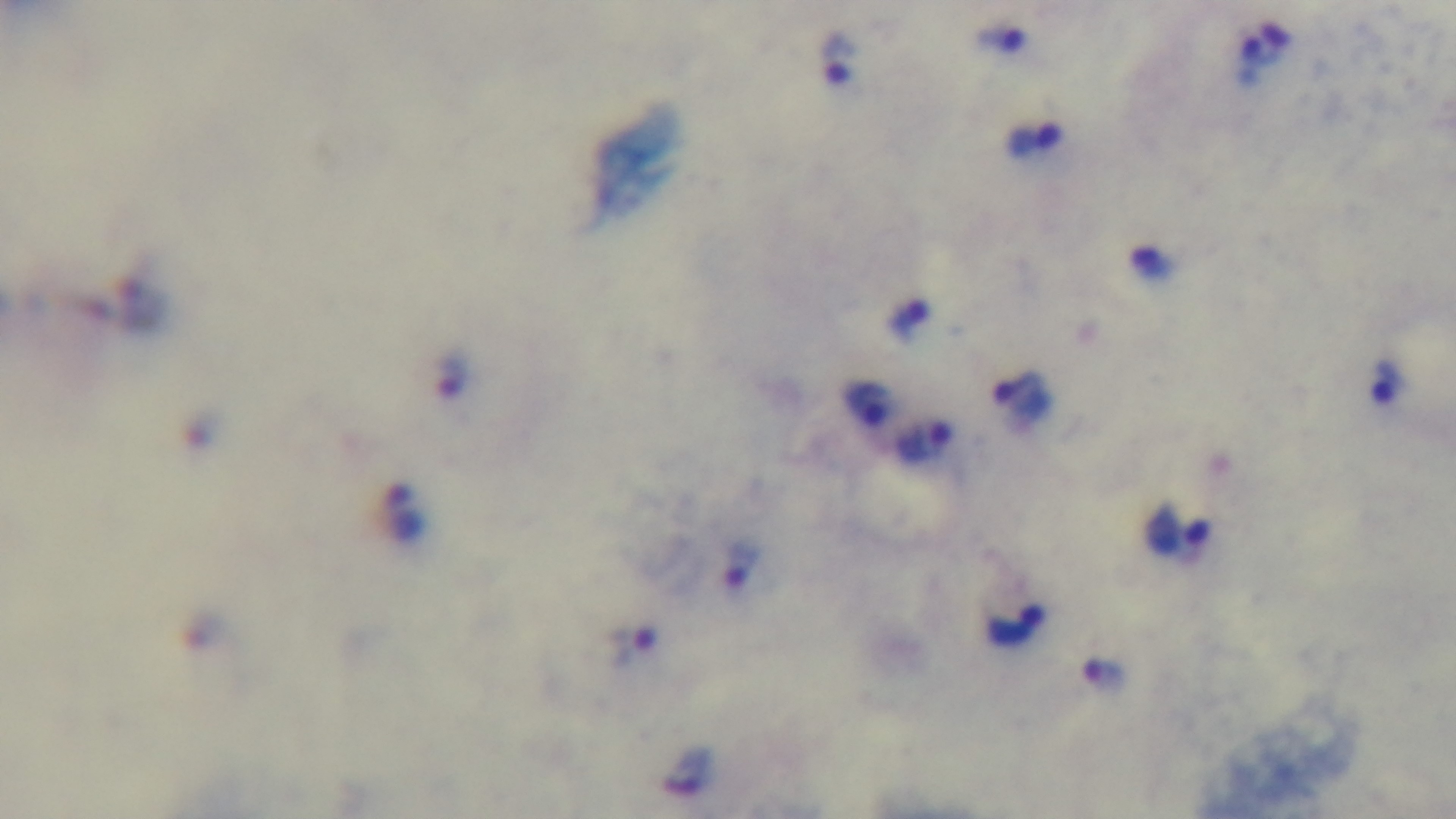
Mounted 4K digital camera. Light microscopy. 100x oil-immersion objective. Giemsa-stained. Malaria status: infected. Single field of view. Preparation: thick blood film.